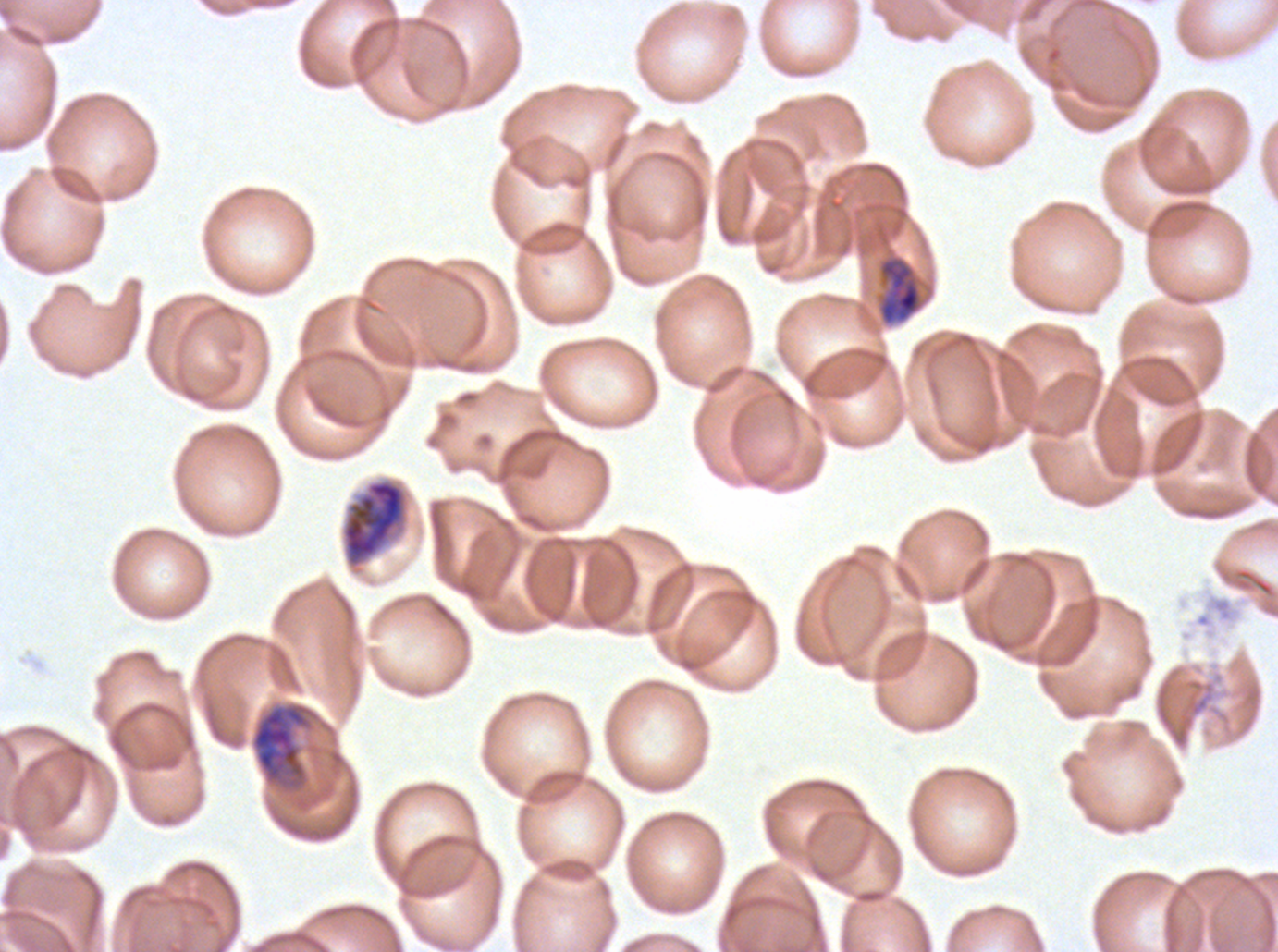

Approximate bounding boxes as (x1, y1, x2, y2) in pixels.
Summary:
  - Late schizont locations: (341, 478, 408, 568)
  - Late trophozoite locations: (250, 700, 322, 798)
  - Mid trophozoite locations: (875, 253, 927, 327)
  - Image size: 1278×952 pixels
  - Life-cycle stages observed: mid trophozoite, late trophozoite, late schizont
  - Specimen: Plasmodium falciparum from a patient in The Gambia, cultured ex vivo for 24 to 48 hours
  - Preparation: thin blood film
  - Field of view: sub-image separated from a larger composite
  - Stain: Giemsa